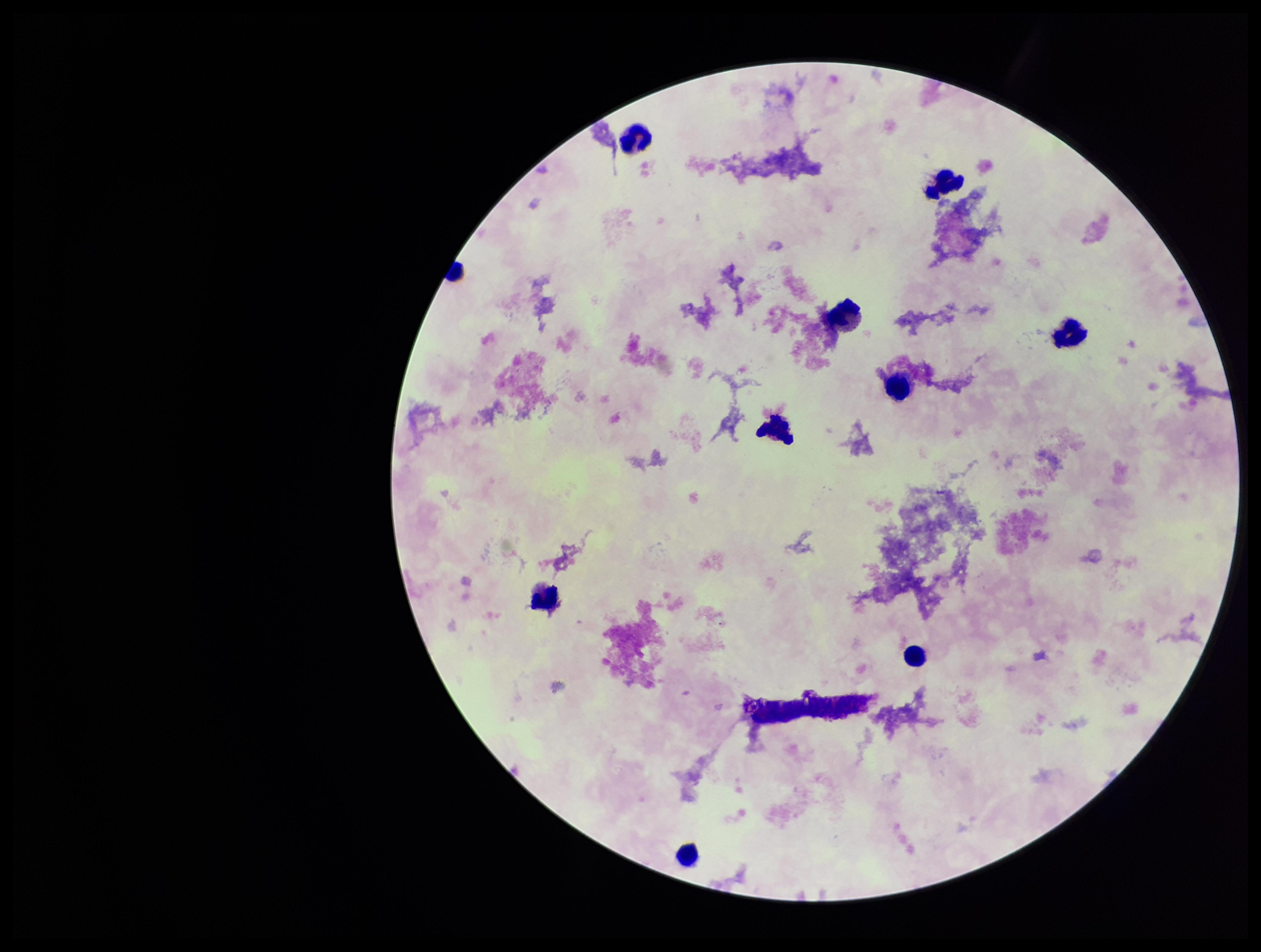

stain = Giemsa
leukocyte count = 10
Plasmodium parasites = none detected
image size = 1261×952 pixels
patient malaria status = negative
parasite count = 0
field of view = one from this slide
capture = smartphone photograph through the microscope eyepiece
preparation = thick smear